Identify the cell.
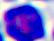
A leukocyte.

magnification = 400x
modality = photomicrograph